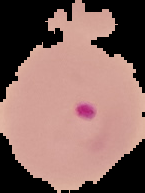

Result: Plasmodium parasites identified. Image is 145×193 pixels. From a thin blood film. The area outside the segmented cell region is set to black.